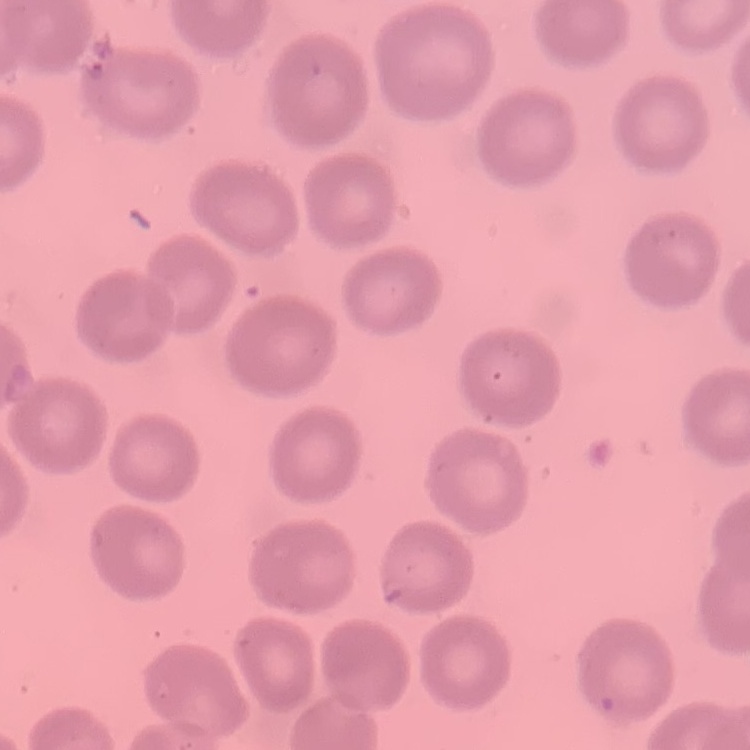
Summary:
  - Erythrocyte morphology: no rouleaux formation
  - Stain: Field's or Giemsa
  - Image type: one tile cut from a larger photomicrograph
  - Preparation: thin blood film